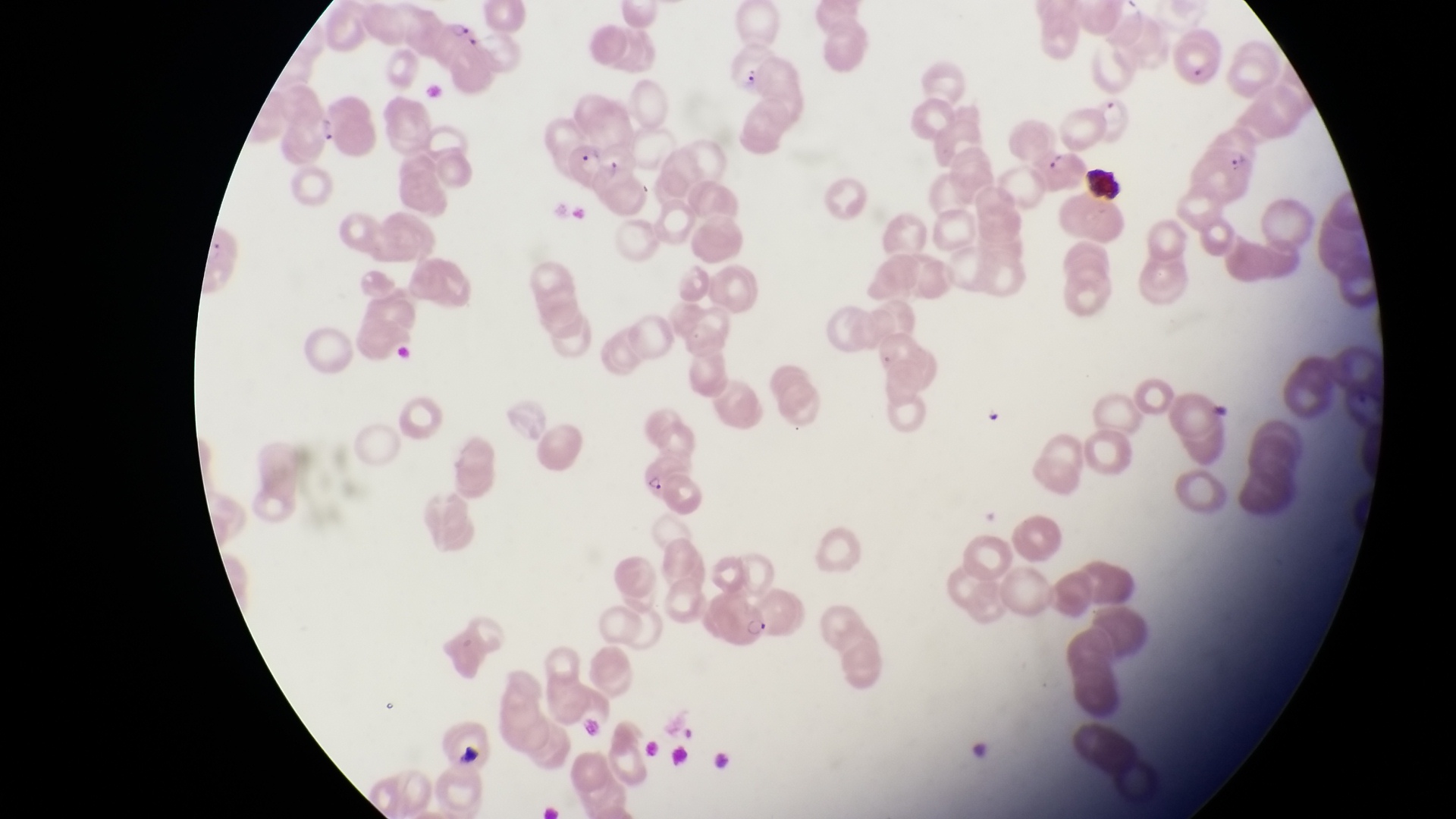
Approximate bounding boxes as {left, top, right, bottom} in pixels. Parasitised red blood cell locations: {436, 18, 481, 68}, {315, 95, 381, 159}, {1096, 98, 1156, 150}, {570, 135, 607, 184}, {1198, 142, 1257, 206}, {1036, 145, 1086, 191}, {645, 450, 703, 521}, {706, 581, 772, 647}. Single field of view. Magnification of 1000x. Sample from Uganda. Captured by a smartphone held over the eyepiece of an Olympus CX-23 microscope. Thin blood film. Image is 1456×819 pixels.